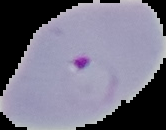

Summary:
  - Preparation: thin blood smear
  - Image type: cell region segmented out of the field of view; surrounding area masked to black
  - Result: malaria parasites detected
  - Image size: 166×130 pixels